Locate every leukocyte (white blood cell).
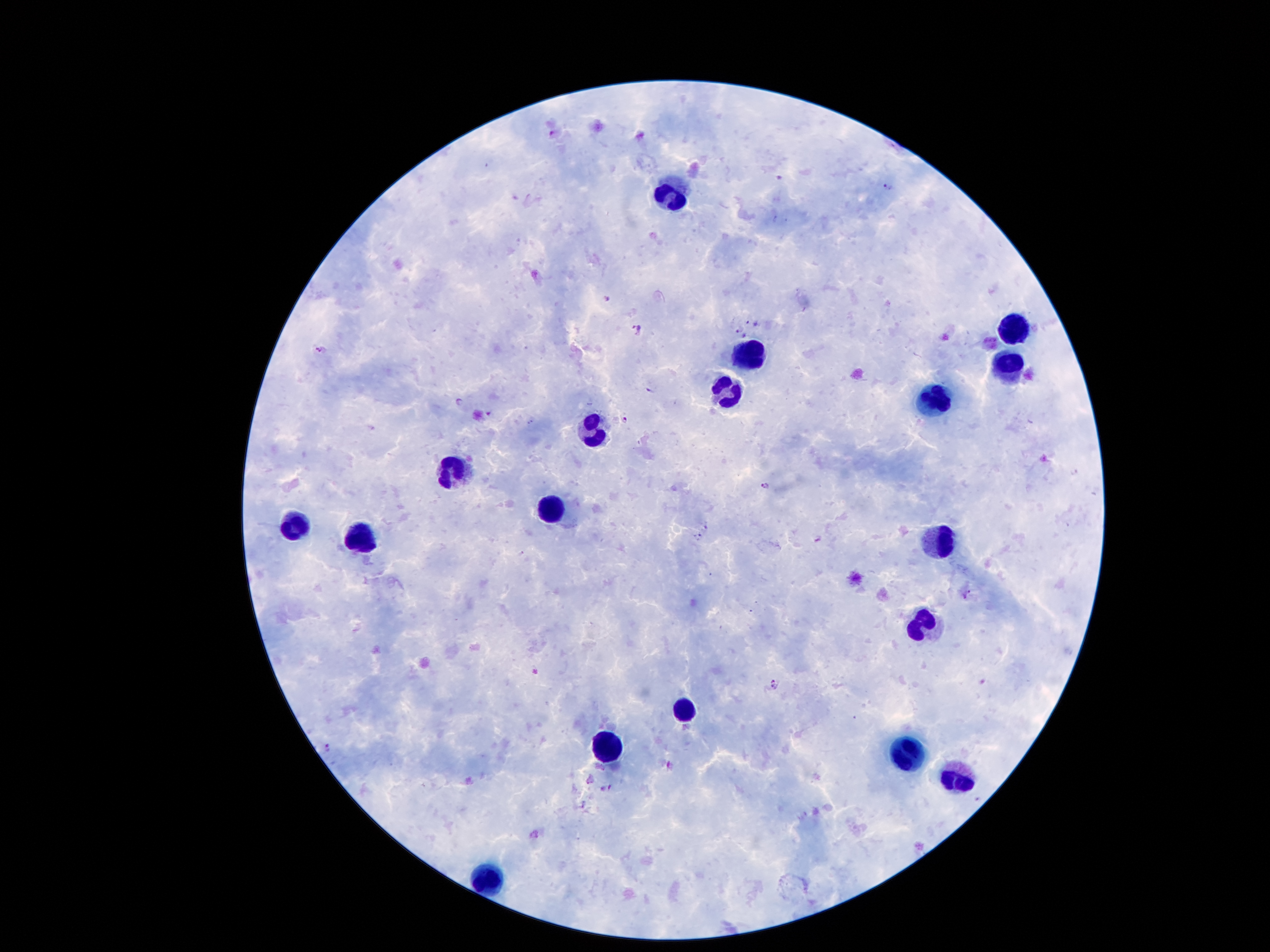

Approximate centers as (x, y) in pixels.
Leukocytes: (667, 191), (1014, 328), (751, 354), (1008, 367), (725, 387), (935, 401), (590, 431), (458, 471), (548, 508), (287, 524), (358, 538), (937, 542), (922, 624), (685, 712), (603, 750), (911, 756), (957, 773), (480, 877).

Plasmodium parasite locations: (552, 133), (779, 179), (888, 186), (607, 299), (747, 319), (637, 330), (738, 330), (744, 334), (320, 349), (650, 387), (461, 401), (625, 419), (531, 421), (1075, 472), (766, 484), (707, 526), (699, 537), (818, 540), (972, 592), (964, 596), (776, 683), (328, 746), (611, 785). 100x magnification. Single field of view. Smartphone photograph taken through the microscope eyepiece. Giemsa-stained preparation. Patient malaria status: positive for Plasmodium falciparum. Image is 1270×952 pixels. Thick peripheral-blood smear.